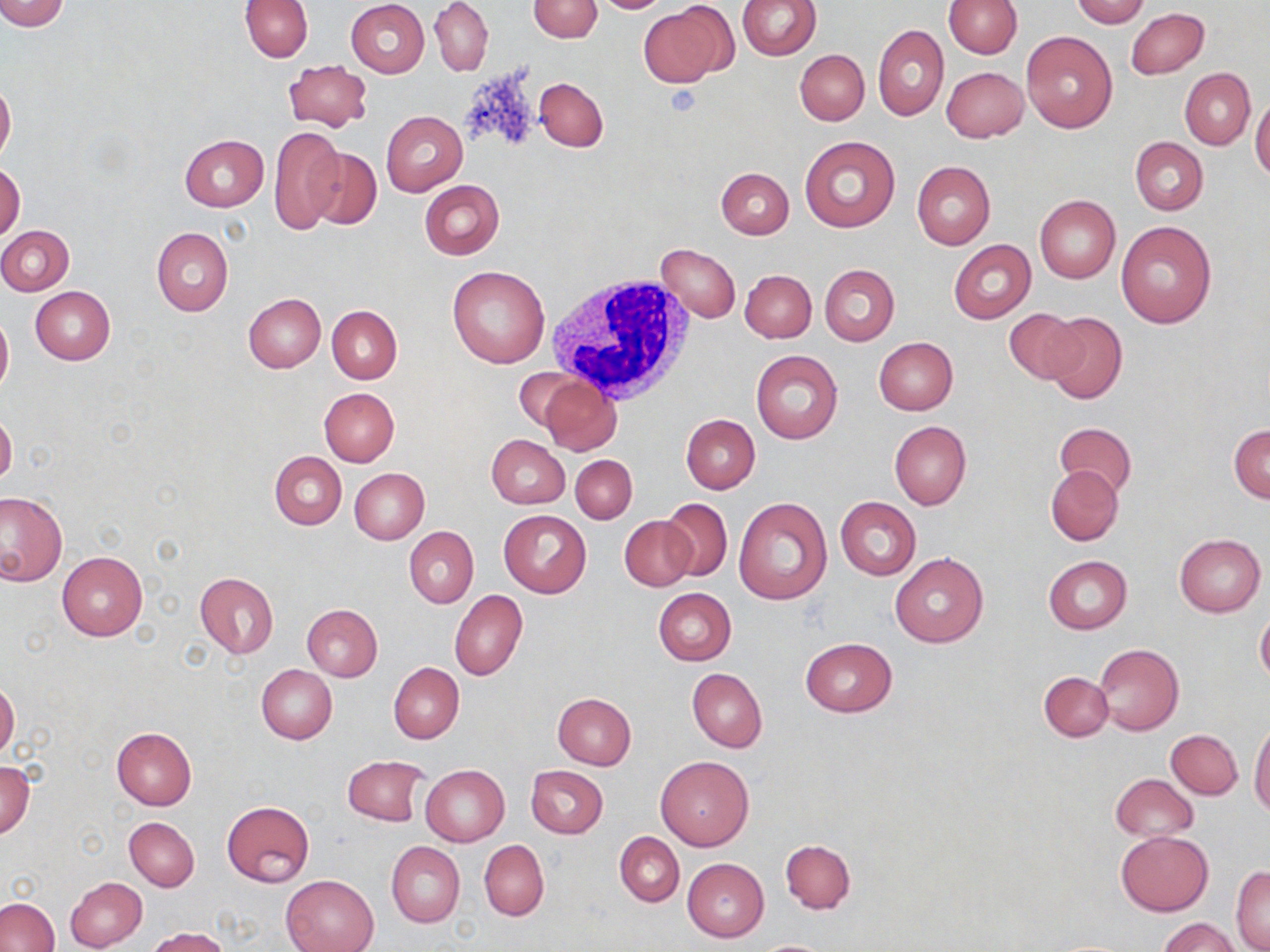
Summary:
  - Coordinate format: approximate bounding boxes as [x1, y1, x2, y2] in pixels
  - Platelet locations: [663, 84, 702, 117]
  - White blood cell locations: [545, 277, 695, 403]
  - Uninfected red blood cell locations: [0, 0, 70, 32], [241, 0, 313, 61], [346, 0, 430, 78], [430, 0, 492, 76], [528, 0, 602, 43], [589, 0, 672, 13], [739, 0, 821, 59], [943, 0, 1020, 58], [1072, 0, 1148, 27], [638, 2, 730, 86], [1126, 7, 1210, 81], [874, 25, 949, 121], [1021, 31, 1117, 134], [794, 49, 869, 125], [282, 59, 372, 131], [942, 66, 1028, 142], [1180, 68, 1255, 149], [535, 77, 608, 151], [0, 79, 15, 163], [1251, 96, 1270, 181], [381, 111, 467, 194], [270, 126, 344, 235], [180, 133, 268, 211], [800, 136, 901, 233], [1130, 136, 1207, 215], [307, 148, 382, 228], [911, 161, 995, 249], [0, 163, 25, 241], [716, 167, 794, 238], [420, 179, 505, 259], [1034, 195, 1120, 283], [1116, 221, 1217, 327], [0, 225, 74, 295], [151, 227, 233, 316], [948, 240, 1035, 323], [656, 243, 741, 323], [820, 264, 899, 345], [447, 265, 551, 368], [740, 269, 816, 343], [30, 285, 116, 364], [244, 293, 325, 372], [328, 306, 401, 382], [1002, 307, 1086, 386], [0, 310, 12, 396], [1041, 311, 1128, 405], [874, 337, 958, 414], [751, 349, 843, 444], [515, 367, 583, 432], [539, 376, 621, 455], [319, 387, 399, 466], [0, 411, 17, 488], [681, 414, 760, 493], [889, 420, 971, 509], [1055, 421, 1137, 496], [1229, 424, 1270, 503], [487, 434, 570, 508], [270, 450, 347, 530], [570, 454, 637, 523], [1046, 464, 1123, 545], [349, 468, 428, 544], [0, 492, 67, 585], [733, 497, 831, 604], [836, 497, 921, 579], [659, 498, 733, 581], [498, 510, 591, 598], [619, 515, 696, 592], [404, 527, 478, 606], [1174, 533, 1265, 616], [56, 551, 148, 641], [890, 552, 988, 647], [1043, 555, 1132, 633], [194, 572, 280, 659], [653, 588, 736, 665], [449, 590, 527, 681], [302, 603, 383, 681], [1255, 610, 1270, 688], [800, 637, 896, 717], [1093, 643, 1184, 735], [388, 662, 463, 743], [256, 664, 337, 744], [687, 668, 767, 752], [1039, 671, 1113, 742], [0, 680, 19, 758], [551, 693, 636, 771], [1249, 722, 1270, 818], [111, 727, 197, 810], [1166, 729, 1242, 799], [655, 754, 754, 851], [342, 756, 429, 827], [1, 761, 35, 838], [420, 764, 510, 846], [527, 765, 608, 838], [1111, 773, 1197, 841], [222, 801, 314, 886], [124, 816, 199, 891], [615, 831, 684, 907], [1115, 831, 1213, 916], [780, 839, 856, 914], [479, 840, 549, 921], [386, 841, 464, 926], [683, 858, 768, 942], [1232, 866, 1270, 952], [282, 875, 378, 952], [65, 876, 146, 951], [0, 898, 59, 952], [1160, 918, 1240, 952], [145, 927, 233, 952], [749, 938, 838, 951]
  - Slide-level diagnosis: negative for blood parasites
  - Field of view: one of a larger specimen
  - Preparation: thin blood smear
  - Stain: May-Grünwald-Giemsa
  - Modality: light microscopy
  - Magnification: 1000x
  - Image size: 1270×952 pixels